Outline each Plasmodium falciparum-infected red blood cell.
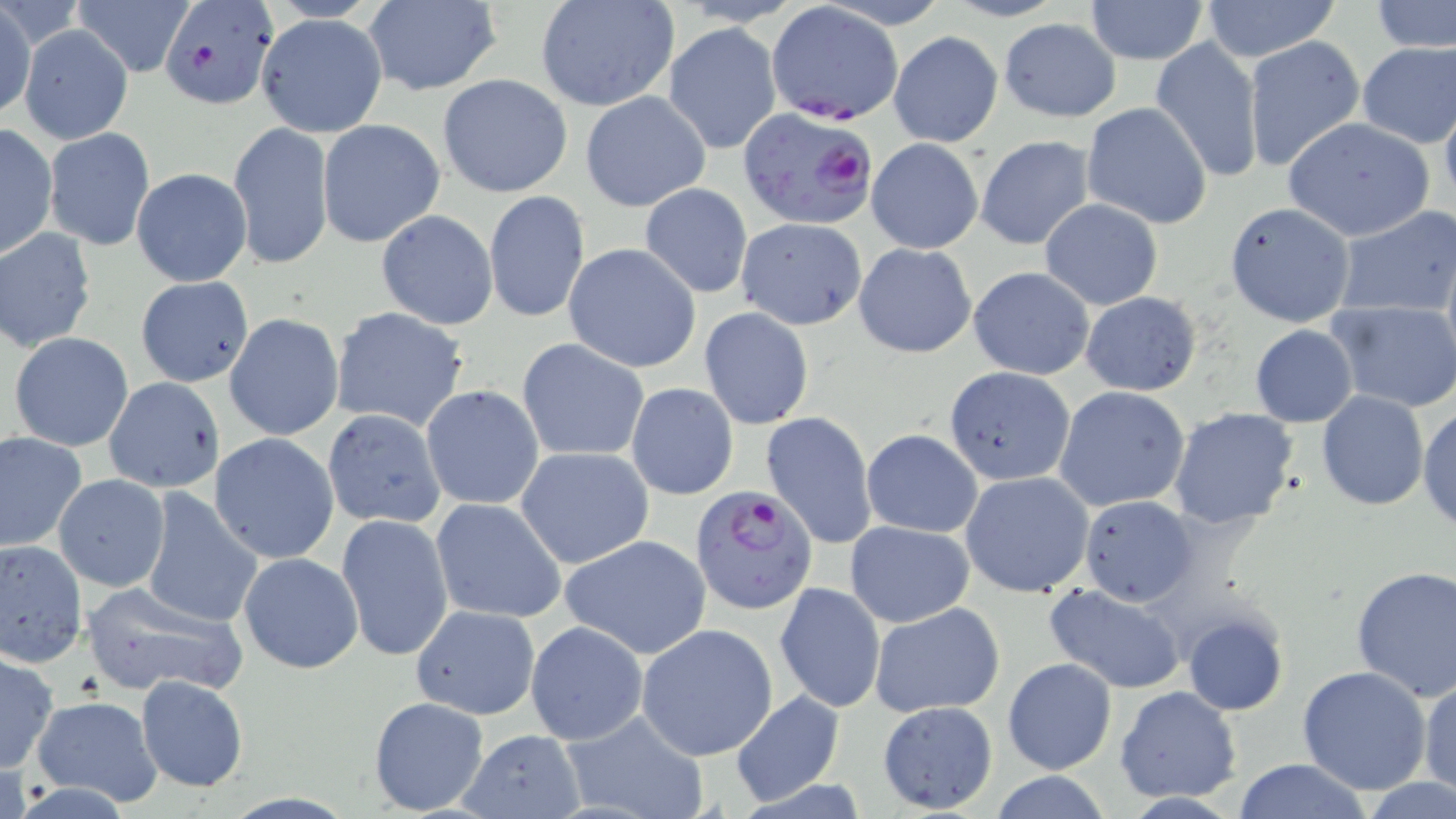

Approximate bounding boxes as (x1, y1, x2, y2) in pixels.
Plasmodium falciparum-infected red blood cells: (157, 0, 275, 111), (765, 3, 904, 126), (738, 107, 879, 232), (692, 484, 815, 612).

Uninfected red blood cell locations: (534, 0, 679, 113), (1084, 0, 1210, 64), (1368, 0, 1456, 54), (74, 1, 191, 76), (361, 1, 501, 95), (1198, 1, 1343, 62), (1, 3, 36, 120), (254, 13, 388, 136), (999, 18, 1120, 121), (662, 23, 782, 154), (20, 25, 132, 145), (888, 30, 1004, 147), (1150, 35, 1267, 180), (1243, 36, 1367, 175), (1356, 42, 1456, 147), (437, 74, 573, 198), (580, 91, 711, 212), (1440, 96, 1456, 213), (1082, 101, 1213, 229), (1283, 118, 1435, 241), (317, 119, 447, 250), (229, 121, 334, 271), (0, 122, 58, 261), (45, 128, 154, 250), (974, 135, 1095, 249), (866, 137, 983, 254), (131, 167, 252, 287), (640, 181, 754, 298), (484, 191, 589, 324), (1039, 197, 1163, 310), (1224, 201, 1355, 327), (1331, 206, 1456, 318), (375, 210, 498, 330), (736, 216, 868, 330), (1, 228, 98, 352), (853, 242, 976, 358), (563, 243, 701, 373), (967, 266, 1094, 379), (134, 275, 253, 388), (1079, 291, 1202, 397), (1329, 302, 1456, 412), (328, 306, 471, 433), (699, 306, 814, 430), (225, 313, 344, 441), (1250, 325, 1359, 427), (8, 332, 134, 453), (519, 338, 649, 463), (944, 366, 1075, 487), (103, 376, 226, 493), (625, 381, 740, 500), (421, 384, 544, 510), (1054, 385, 1190, 513), (1315, 390, 1429, 511), (1417, 404, 1456, 532), (1168, 406, 1301, 529), (322, 408, 447, 530), (760, 411, 877, 550), (860, 429, 983, 538), (1, 431, 87, 552), (209, 433, 339, 565), (517, 447, 653, 569), (960, 471, 1094, 598), (53, 475, 169, 591), (138, 487, 263, 628), (1078, 495, 1199, 607), (431, 497, 568, 623), (335, 513, 453, 663), (845, 521, 975, 628), (559, 535, 711, 659), (0, 540, 87, 668), (238, 553, 363, 674), (1350, 565, 1456, 701), (79, 581, 249, 699), (775, 582, 886, 713), (1041, 583, 1189, 693), (409, 603, 539, 719), (870, 603, 1006, 718), (1181, 610, 1290, 718), (525, 621, 647, 746), (637, 624, 779, 761), (0, 651, 58, 773), (1002, 656, 1117, 777), (1298, 664, 1432, 795), (136, 675, 248, 793), (1417, 676, 1455, 799), (1115, 685, 1242, 803), (729, 691, 846, 807), (31, 696, 162, 808), (368, 696, 490, 814), (875, 701, 999, 814), (565, 709, 712, 819), (456, 729, 586, 818), (1229, 759, 1376, 818), (1361, 778, 1456, 818). Slide-level diagnosis: Plasmodium falciparum. May-Grünwald-Giemsa-stained preparation. Light microscopy. Single field of view. Image is 1456×819 pixels. 1000x magnification. Thin blood film.